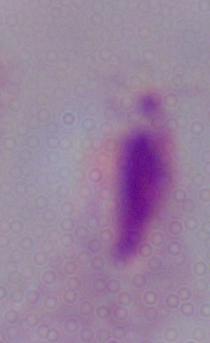

Summary:
  - Modality: photomicrograph
  - Magnification: 1000x
  - Identification: trichomonad